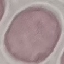

Summary:
  - Result: no malaria parasites detected
  - Preparation: thin smear
  - Stain: Giemsa
  - Image type: automatically extracted cell patch, resized to 64 × 64 pixels
  - Capture: smartphone camera at the microscope eyepiece